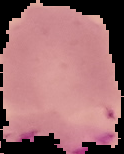
result: malaria parasites detected
preparation: thin blood film
image_type: segmented cell region with the area outside set to black
image_size: 124×154 pixels